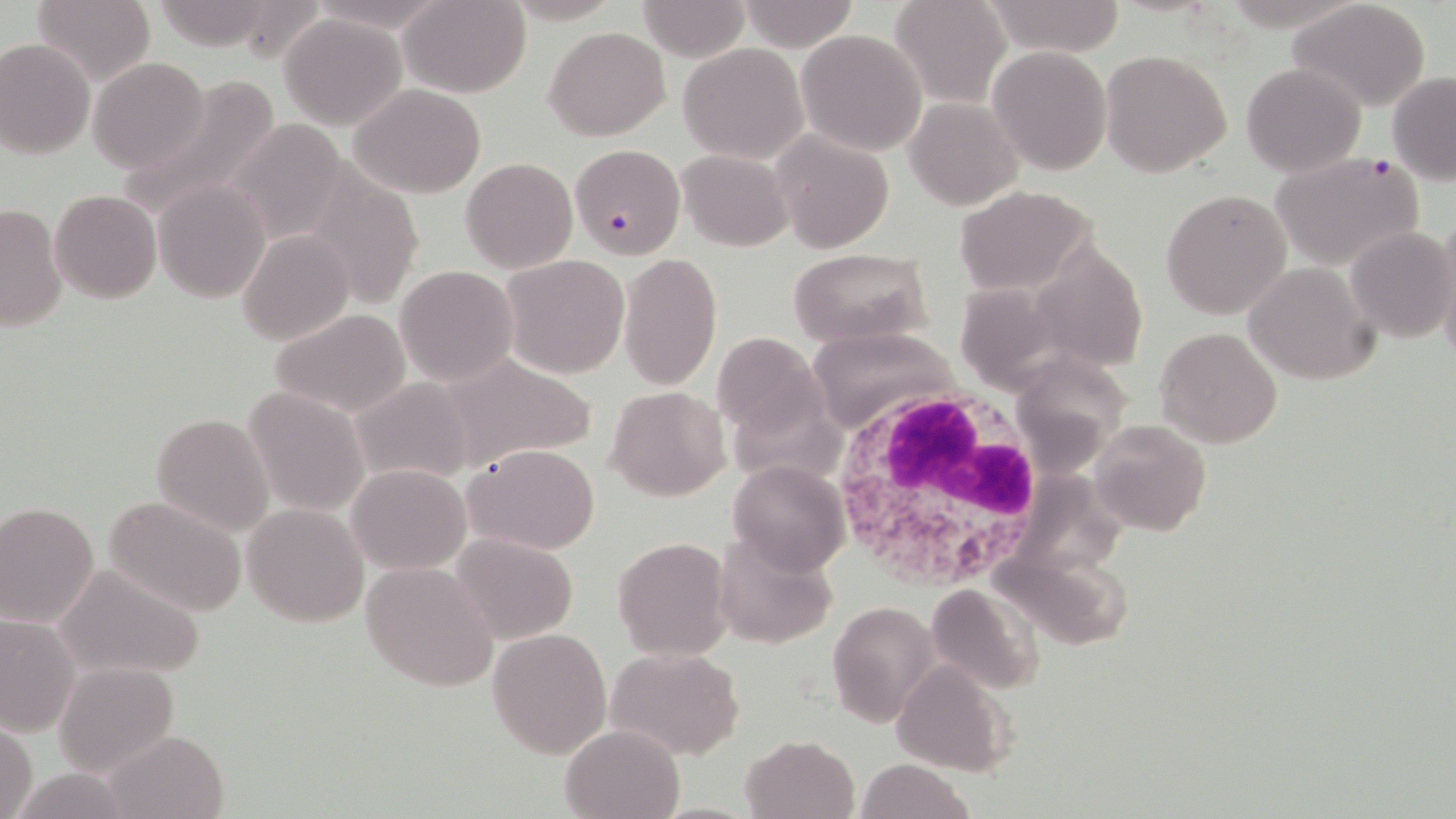

slide_level_diagnosis: Plasmodium falciparum
stain: May-Grünwald-Giemsa
image_size: 1456×819 pixels
modality: light microscopy
uninfected_red_blood_cell_locations: 'approximate bounding boxes as (x1,y1)-(x2,y2) corner pairs in pixels: (399,0)-(530,97), (737,0)-(858,48), (890,0)-(1012,109), (636,1)-(752,60), (1291,1)-(1432,111), (31,2)-(154,82), (982,2)-(1126,57), (279,13)-(407,129), (545,26)-(671,141), (795,29)-(927,155), (0,37)-(95,158), (678,43)-(808,163), (987,45)-(1112,174), (1100,48)-(1233,179), (87,56)-(211,175), (1241,62)-(1366,177), (1387,72)-(1455,184), (112,79)-(281,217), (348,84)-(485,198), (904,98)-(1022,209), (226,120)-(352,245), (769,128)-(896,255), (676,149)-(794,251), (461,157)-(577,271), (299,167)-(426,310), (153,180)-(268,302), (953,183)-(1098,297), (1160,188)-(1295,320), (49,190)-(162,303), (0,202)-(66,334), (1432,224)-(1456,358), (1346,225)-(1455,342), (237,228)-(355,345), (1051,234)-(1149,374), (787,248)-(933,348), (616,253)-(721,394), (501,255)-(630,379), (1246,261)-(1380,385), (963,264)-(1075,387), (395,265)-(520,386), (269,309)-(413,419), (1155,325)-(1283,448), (806,327)-(961,433), (711,331)-(828,442), (1024,344)-(1126,469), (435,355)-(597,473), (350,376)-(480,488), (604,384)-(730,500), (243,386)-(370,517), (151,412)-(274,535), (1090,417)-(1211,537), (465,442)-(601,554), (728,458)-(850,576), (347,463)-(471,574), (1007,469)-(1131,570), (101,493)-(248,618), (0,501)-(100,627), (242,502)-(368,627), (712,530)-(838,649), (453,533)-(579,644), (612,535)-(732,661), (1000,554)-(1137,660), (52,561)-(206,679), (361,561)-(499,692), (927,582)-(1041,697), (827,600)-(941,729), (0,616)-(78,737), (488,627)-(613,760), (605,646)-(745,759), (890,657)-(1016,775), (53,660)-(180,778), (0,723)-(38,819), (560,723)-(687,819), (102,727)-(229,817), (740,733)-(861,819), (855,758)-(974,819), (13,768)-(135,818)'
preparation: thin blood film
plasmodium_falciparum_infected_red_blood_cell_locations: 'approximate bounding boxes as (x1,y1)-(x2,y2) corner pairs in pixels: (570,143)-(685,258), (1267,153)-(1426,270)'
white_blood_cell_locations: 'approximate bounding boxes as (x1,y1)-(x2,y2) corner pairs in pixels: (826,385)-(1048,590)'
magnification: 1000x
field_of_view: single